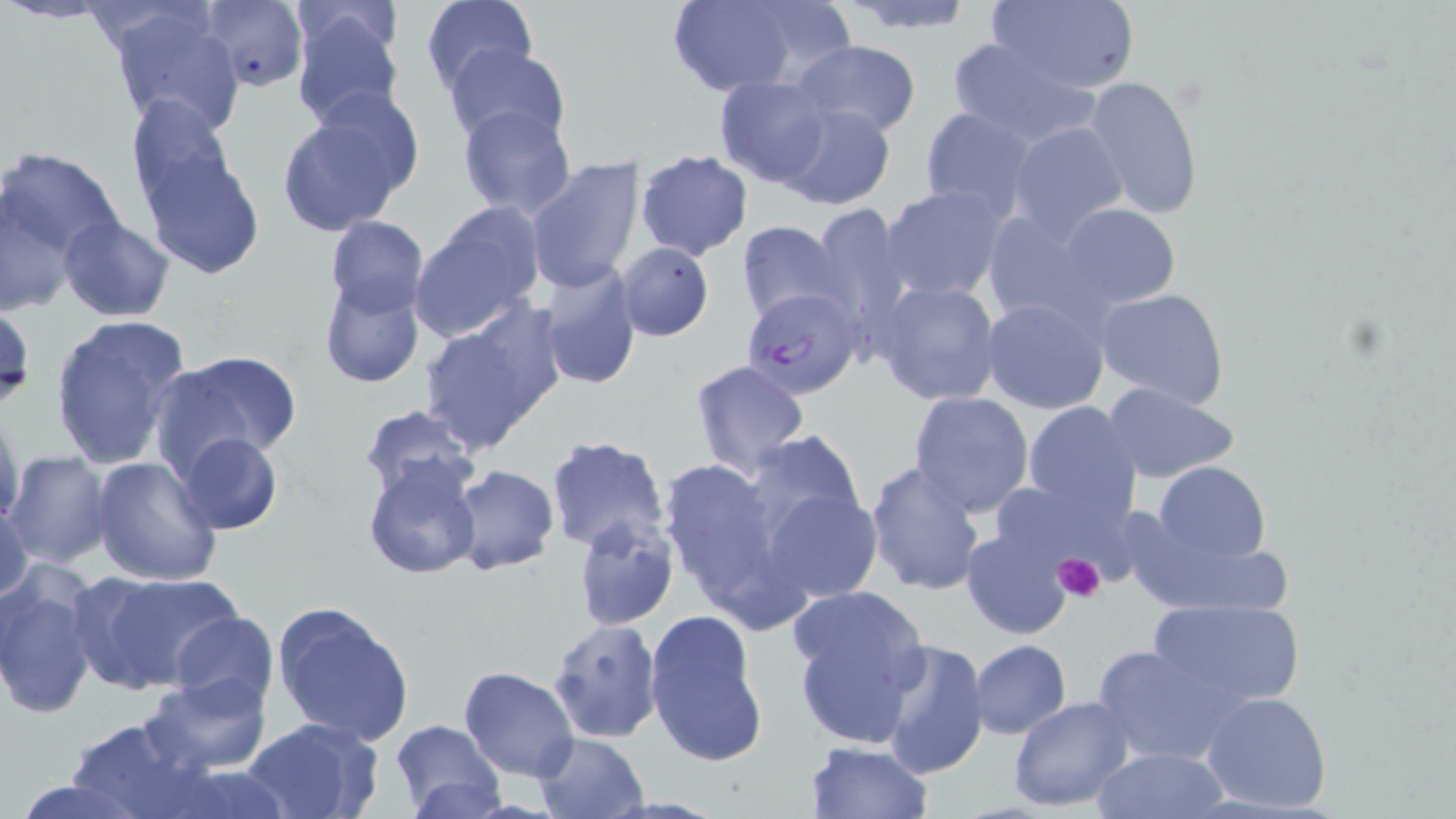 Approximate bounding boxes as (x1,y1)-(x2,y2) corner pairs in pixels. Platelet locations: (1054,554)-(1108,605). Plasmodium falciparum-infected red blood cell locations: (742,287)-(864,399). Uninfected red blood cell locations: (196,0)-(307,93), (421,0)-(534,93), (663,0)-(812,97), (836,0)-(980,34), (987,0)-(1140,92), (105,4)-(248,137), (289,4)-(406,130), (946,36)-(1095,147), (792,39)-(921,139), (443,43)-(570,148), (1084,74)-(1203,222), (715,75)-(833,187), (277,96)-(419,234), (124,99)-(246,230), (773,102)-(898,211), (458,103)-(577,222), (919,106)-(1037,219), (1009,121)-(1129,241), (141,143)-(265,278), (0,145)-(125,263), (635,150)-(753,260), (523,157)-(643,294), (880,184)-(1009,301), (0,187)-(83,316), (410,204)-(546,340), (806,204)-(912,329), (1058,204)-(1178,308), (980,209)-(1107,328), (58,214)-(178,324), (325,214)-(429,318), (737,220)-(846,324), (615,241)-(714,342), (538,261)-(642,390), (319,277)-(425,390), (875,281)-(1002,406), (1095,288)-(1232,410), (980,296)-(1111,416), (0,300)-(36,415), (417,302)-(566,454), (47,312)-(191,473), (149,350)-(301,478), (688,360)-(812,480), (1101,382)-(1243,484), (908,390)-(1034,516), (1021,401)-(1142,523), (356,402)-(479,502), (1,405)-(25,527), (743,429)-(870,543), (177,430)-(283,534), (546,434)-(669,553), (4,452)-(113,568), (656,455)-(795,618), (91,456)-(222,587), (363,457)-(482,579), (863,459)-(987,596), (1148,461)-(1274,573), (448,465)-(559,575), (760,482)-(886,604), (1,495)-(35,604), (571,511)-(682,632), (962,528)-(1074,641), (0,564)-(101,721), (74,568)-(245,696), (788,585)-(929,749), (1144,595)-(1306,714), (270,600)-(414,745), (643,609)-(769,771), (167,611)-(279,711), (546,617)-(665,744), (876,638)-(989,776), (969,639)-(1071,738), (1091,641)-(1237,765), (459,666)-(579,781), (142,671)-(272,774), (1200,690)-(1334,812), (1008,694)-(1136,813), (242,715)-(385,819), (65,716)-(206,819), (389,719)-(505,819), (533,733)-(650,819), (806,741)-(933,819), (1090,745)-(1229,818), (148,760)-(300,819), (6,775)-(160,819). Slide-level diagnosis: Plasmodium falciparum. Light microscopy. One field of a larger specimen. Image is 1456×819 pixels. 1000x magnification. May-Grünwald-Giemsa stain. Thin blood smear.